State which parasite is depicted.
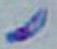
Toxoplasma gondii.

Summary:
  - Modality: micrograph
  - Magnification: 1000x